Classify this cell by malaria status.
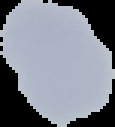
It is uninfected.

image size = 115×127 pixels
image type = segmented cell region with the area outside set to black
preparation = thin blood film